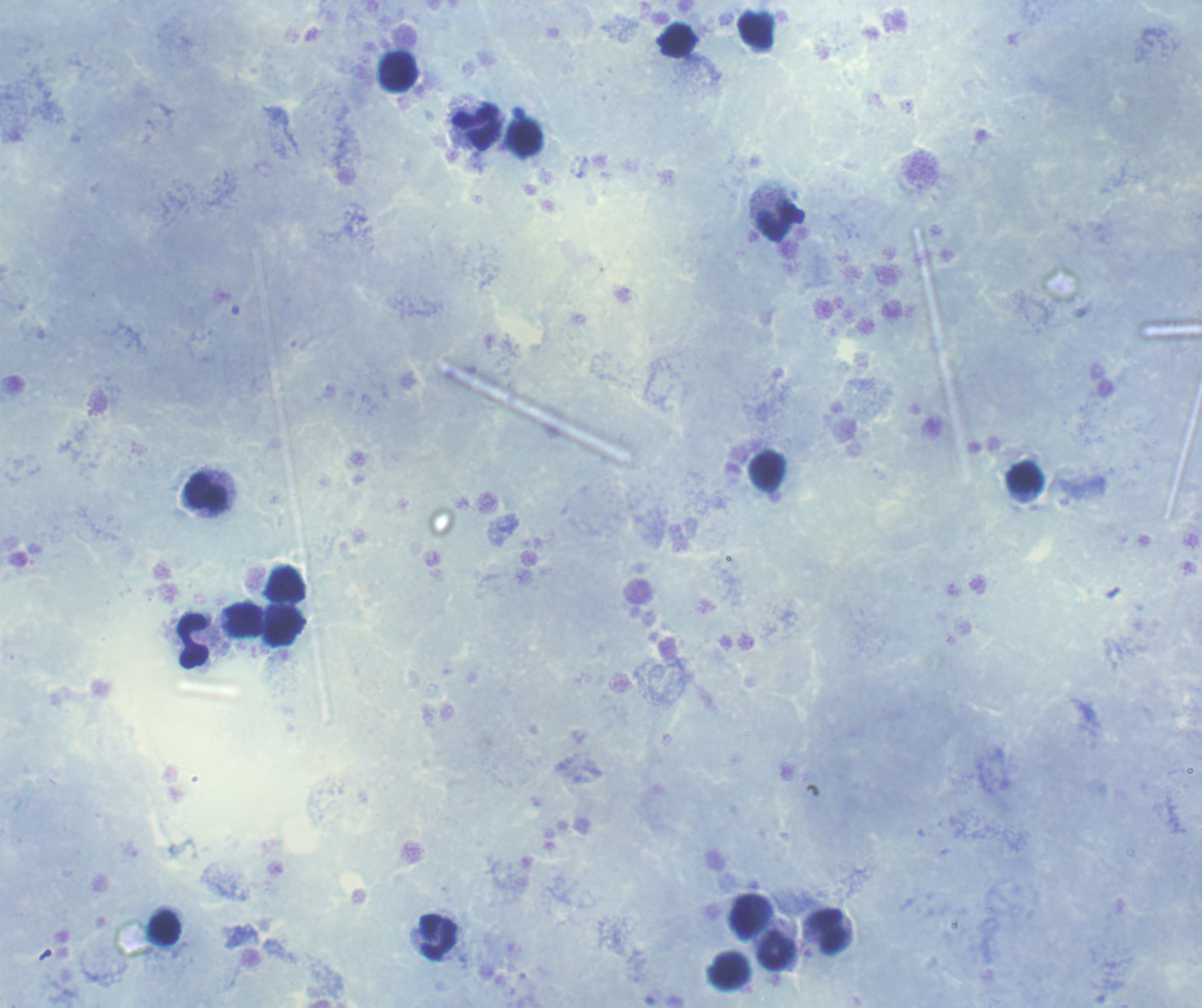
{
  "stain": "Romanowsky",
  "coloration_quality": "good",
  "leukocyte_locations": "approximate centers as [x, y] in pixels: [756, 30], [678, 41], [398, 72], [476, 127], [779, 222], [1025, 479], [207, 493], [244, 622], [284, 626], [193, 641], [165, 929], [831, 931], [438, 936], [777, 952]",
  "field_of_view": "single",
  "context": "previously used in an actual diagnosis",
  "result": "negative for malaria parasites",
  "magnification": "100x",
  "background_quality": "good",
  "preparation": "thick smear of blood",
  "image_size": "1202×1008 pixels"
}